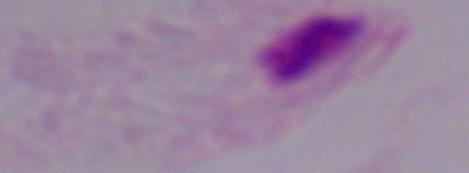

A trichomonad is shown. Photomicrograph. Captured at 1000x magnification.